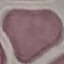
{
  "result": "no malaria parasites detected",
  "image_type": "cell patch, automatically extracted from a larger field of view and resized to 64 × 64 pixels",
  "capture": "smartphone camera at the microscope eyepiece",
  "stain": "Giemsa",
  "preparation": "thin blood film"
}